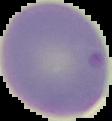
result: Plasmodium parasites identified
image_type: cell region segmented out of the field of view; surrounding area masked to black
image_size: 112×121 pixels
preparation: thin blood smear